Point out each leukocyte.
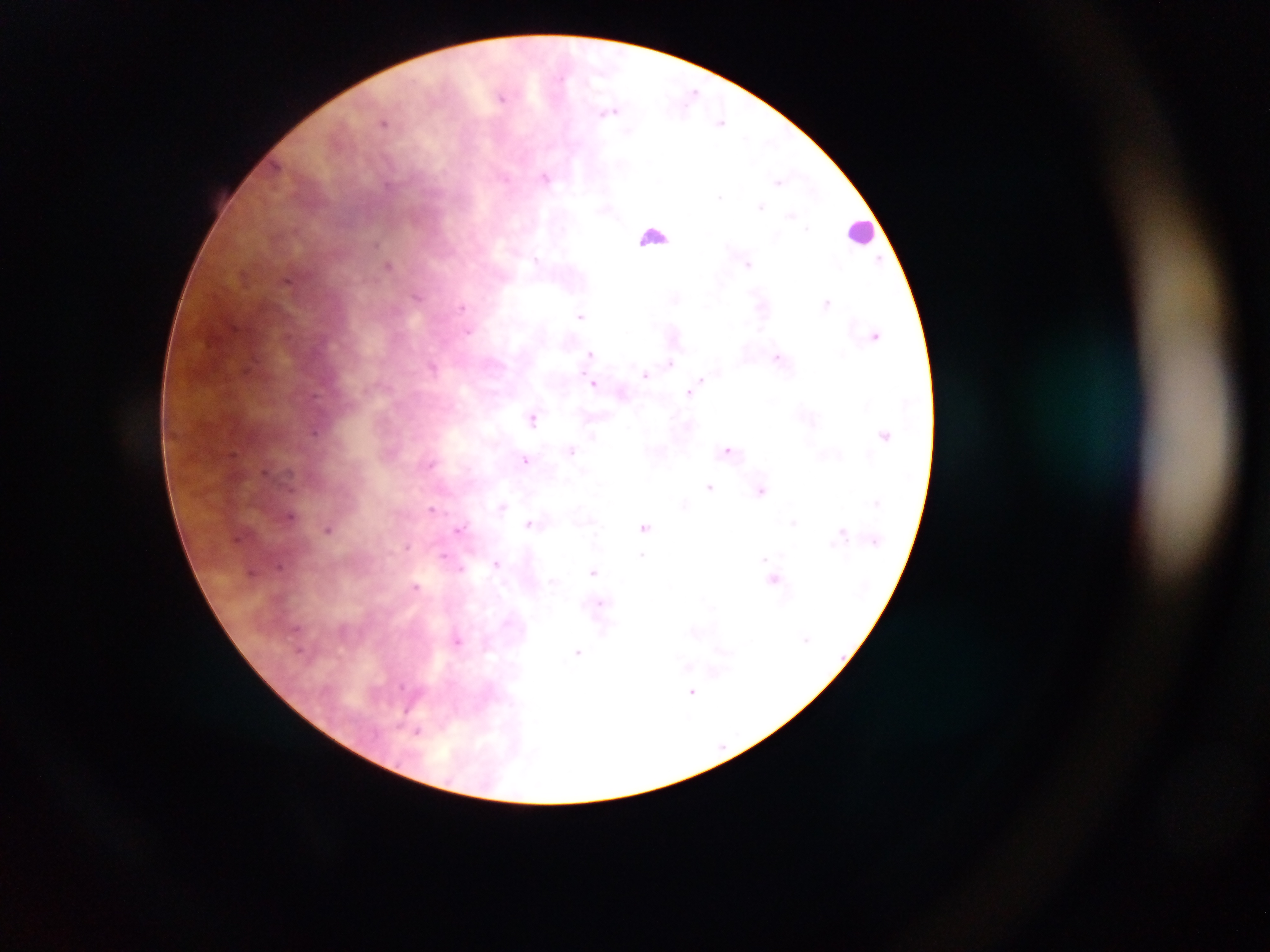
Approximate centers as [x, y] in pixels.
Leukocytes: [862, 231], [654, 235].

Summary:
  - Malaria parasite locations: [694, 91], [501, 97], [611, 112], [383, 122], [721, 123], [546, 177], [505, 178], [778, 181], [388, 186], [721, 197], [761, 206], [791, 215], [807, 228], [376, 243], [537, 258], [880, 259], [747, 264], [389, 265], [287, 282], [418, 296], [827, 302], [462, 307], [580, 315], [468, 331], [876, 335], [590, 353], [777, 357], [670, 363], [250, 367], [432, 368], [645, 375], [701, 379], [594, 383], [689, 392], [314, 397], [532, 418], [314, 431], [593, 436], [727, 449], [571, 450], [526, 459], [430, 464], [265, 472], [710, 487], [761, 490], [501, 506], [431, 509], [290, 515], [794, 522], [529, 523], [645, 527], [328, 528], [459, 528], [842, 532], [237, 538], [407, 546], [444, 554], [642, 554], [764, 558], [497, 563], [279, 565], [461, 568], [594, 571], [251, 572], [774, 579], [416, 586], [600, 603], [296, 629], [602, 631], [458, 641], [299, 650], [577, 652], [692, 692], [418, 732]
  - Country: Ghana
  - Image size: 1270×952 pixels
  - Field of view: single
  - Capture: mobile-phone photograph through a microscope
  - Preparation: thick blood smear